Give the extent of all white blood cells.
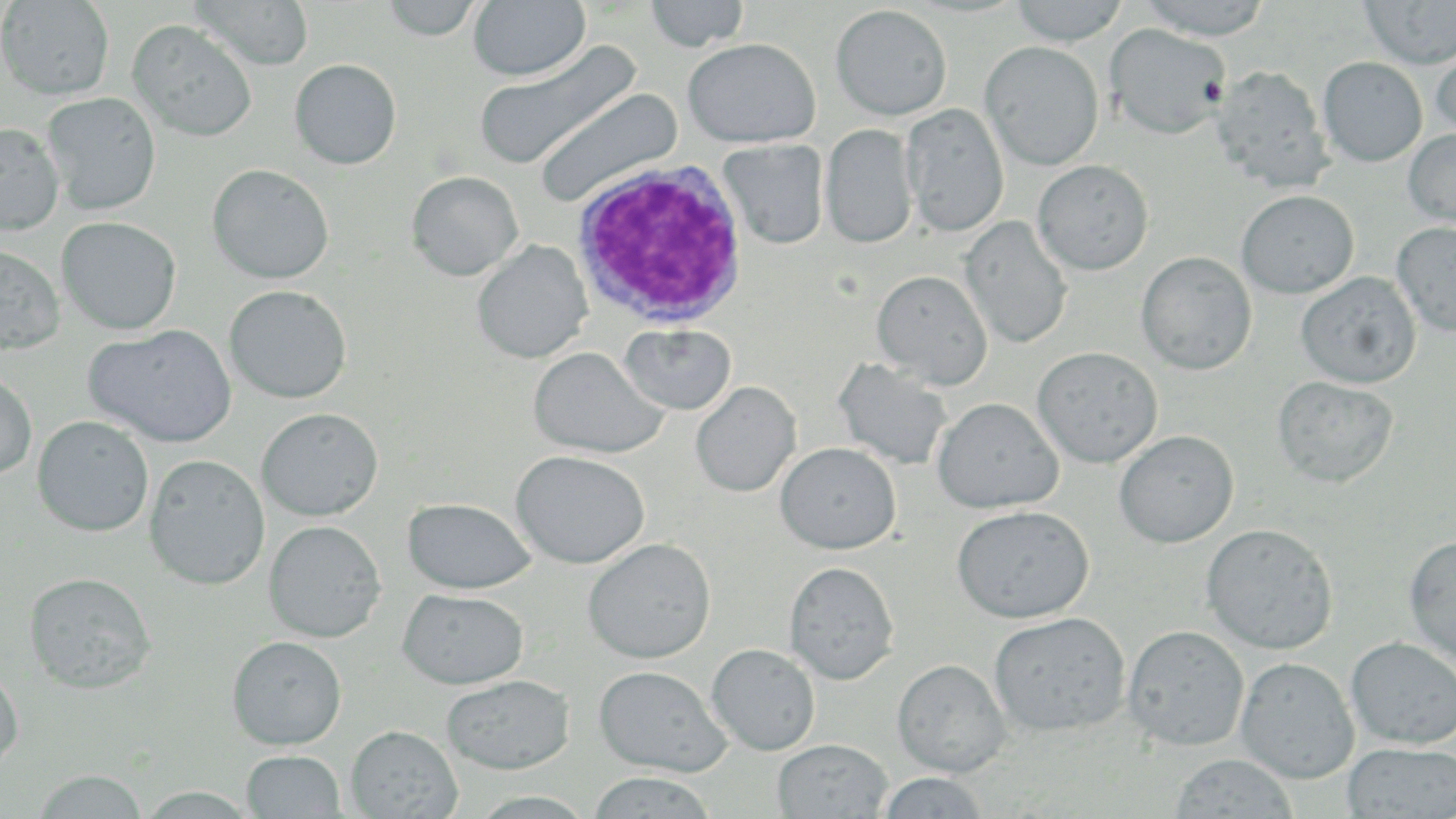

Approximate bounding boxes as (x1,y1)-(x2,y2) corner pairs in pixels.
White blood cells: (571,159)-(748,331).

slide-level diagnosis = Plasmodium ovale
uninfected red blood cell locations = approximate bounding boxes as (x1,y1)-(x2,y2) corner pairs in pixels: (0,0)-(114,100), (188,0)-(315,70), (380,0)-(485,41), (469,0)-(590,82), (644,0)-(750,52), (1009,0)-(1129,46), (1137,0)-(1273,40), (1358,1)-(1456,70), (830,4)-(952,121), (128,20)-(257,142), (1105,23)-(1231,139), (683,38)-(821,147), (1431,38)-(1456,142), (473,40)-(643,171), (980,41)-(1104,171), (1317,57)-(1427,167), (290,59)-(402,170), (1211,64)-(1332,192), (533,87)-(683,207), (42,93)-(161,215), (901,103)-(1009,236), (0,122)-(64,235), (821,124)-(918,249), (1403,128)-(1456,229), (718,139)-(829,249), (1033,160)-(1154,275), (207,164)-(334,284), (407,171)-(523,280), (1236,190)-(1358,298), (57,216)-(182,335), (961,216)-(1072,349), (1391,222)-(1456,339), (472,240)-(592,363), (0,244)-(65,354), (1136,251)-(1257,375), (871,269)-(993,389), (1296,272)-(1421,388), (223,285)-(352,404), (619,323)-(737,415), (85,324)-(237,448), (528,346)-(667,459), (1032,346)-(1163,468), (832,358)-(955,471), (0,371)-(37,480), (1272,375)-(1399,488), (690,381)-(801,497), (932,397)-(1063,513), (256,408)-(383,521), (32,416)-(154,536), (1114,430)-(1239,548), (775,442)-(901,555), (511,450)-(649,569), (144,454)-(269,590), (402,498)-(537,593), (951,505)-(1094,623), (264,520)-(386,643), (1201,523)-(1339,654), (1404,537)-(1456,667), (583,538)-(716,664), (784,561)-(899,685), (23,571)-(157,693), (397,589)-(529,689), (988,612)-(1131,737), (1122,625)-(1249,750), (227,636)-(347,749), (1345,637)-(1456,748), (707,643)-(821,755), (1235,657)-(1359,783), (892,659)-(1011,777), (593,665)-(731,776), (0,666)-(23,774), (441,674)-(575,774), (346,725)-(462,818), (773,739)-(893,818), (1343,743)-(1456,818), (241,750)-(346,818), (1169,752)-(1298,817), (31,770)-(149,818), (586,772)-(717,818), (877,772)-(990,818), (138,787)-(259,818), (467,791)-(598,818)
stain = May-Grünwald-Giemsa
preparation = thin blood smear
image size = 1456×819 pixels
modality = light microscopy
field of view = single
magnification = 1000x